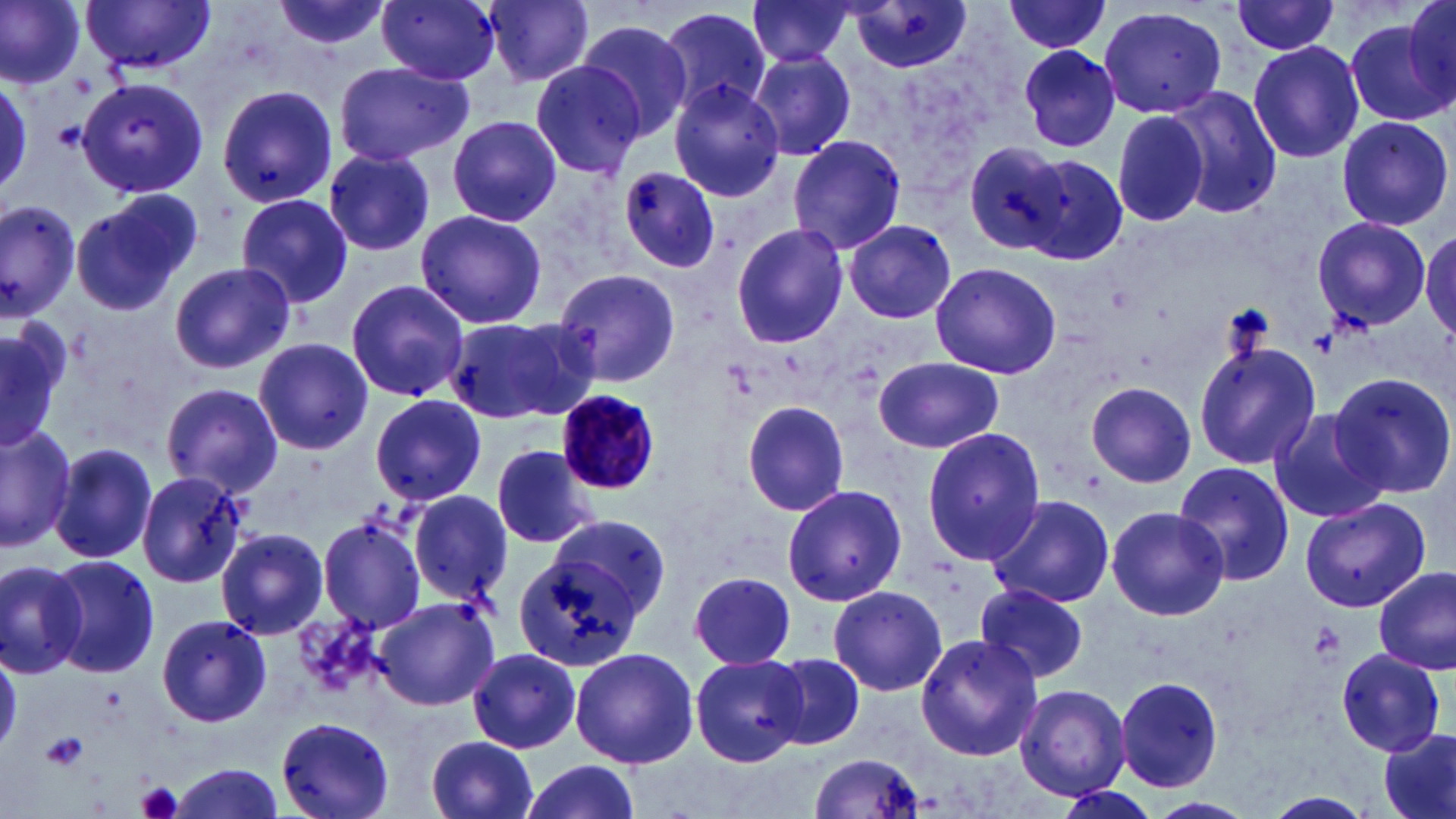
slide-level diagnosis = Plasmodium malariae
preparation = thin blood smear
modality = optical microscopy
field of view = single
platelet locations = approximate bounding boxes as named x1/y1/x2/y2 corners in pixels: (x1=54, y1=121, x2=86, y2=151), (x1=1309, y1=327, x2=1340, y2=356), (x1=1306, y1=623, x2=1344, y2=663), (x1=40, y1=732, x2=88, y2=770), (x1=134, y1=781, x2=185, y2=819)
magnification = 1000x
Plasmodium malariae-infected red blood cell locations = approximate bounding boxes as named x1/y1/x2/y2 corners in pixels: (x1=554, y1=388, x2=662, y2=496)
image size = 1456×819 pixels
uninfected red blood cell locations = approximate bounding boxes as named x1/y1/x2/y2 corners in pixels: (x1=0, y1=0, x2=87, y2=90), (x1=269, y1=0, x2=398, y2=55), (x1=378, y1=0, x2=502, y2=84), (x1=1403, y1=0, x2=1456, y2=104), (x1=83, y1=1, x2=218, y2=77), (x1=483, y1=1, x2=595, y2=86), (x1=1001, y1=1, x2=1114, y2=54), (x1=745, y1=2, x2=856, y2=66), (x1=1230, y1=2, x2=1342, y2=56), (x1=848, y1=4, x2=975, y2=74), (x1=1097, y1=5, x2=1229, y2=120), (x1=656, y1=6, x2=773, y2=121), (x1=1343, y1=14, x2=1452, y2=130), (x1=576, y1=22, x2=694, y2=142), (x1=1247, y1=41, x2=1364, y2=164), (x1=1017, y1=45, x2=1121, y2=153), (x1=748, y1=49, x2=857, y2=162), (x1=331, y1=60, x2=473, y2=166), (x1=528, y1=60, x2=648, y2=178), (x1=0, y1=75, x2=32, y2=196), (x1=77, y1=76, x2=210, y2=199), (x1=669, y1=81, x2=786, y2=202), (x1=216, y1=84, x2=339, y2=210), (x1=1164, y1=87, x2=1280, y2=218), (x1=1111, y1=110, x2=1208, y2=229), (x1=1335, y1=114, x2=1454, y2=232), (x1=447, y1=115, x2=562, y2=227), (x1=788, y1=134, x2=906, y2=254), (x1=960, y1=144, x2=1071, y2=254), (x1=322, y1=150, x2=441, y2=258), (x1=1015, y1=153, x2=1129, y2=267), (x1=617, y1=166, x2=723, y2=274), (x1=75, y1=189, x2=204, y2=314), (x1=235, y1=193, x2=354, y2=308), (x1=0, y1=201, x2=80, y2=320), (x1=414, y1=209, x2=549, y2=330), (x1=1311, y1=216, x2=1431, y2=328), (x1=843, y1=220, x2=957, y2=325), (x1=730, y1=223, x2=848, y2=349), (x1=1421, y1=226, x2=1456, y2=343), (x1=168, y1=261, x2=295, y2=374), (x1=927, y1=261, x2=1062, y2=380), (x1=551, y1=266, x2=684, y2=391), (x1=345, y1=279, x2=471, y2=403), (x1=444, y1=315, x2=594, y2=425), (x1=0, y1=320, x2=65, y2=456), (x1=253, y1=337, x2=372, y2=456), (x1=1194, y1=338, x2=1321, y2=468), (x1=874, y1=354, x2=1003, y2=453), (x1=1327, y1=373, x2=1456, y2=500), (x1=161, y1=381, x2=283, y2=497), (x1=1083, y1=381, x2=1197, y2=489), (x1=370, y1=393, x2=486, y2=505), (x1=741, y1=400, x2=848, y2=517), (x1=1267, y1=409, x2=1391, y2=524), (x1=0, y1=424, x2=78, y2=553), (x1=921, y1=426, x2=1046, y2=565), (x1=49, y1=441, x2=157, y2=565), (x1=492, y1=444, x2=600, y2=550), (x1=1172, y1=462, x2=1295, y2=587), (x1=136, y1=470, x2=249, y2=589), (x1=781, y1=483, x2=907, y2=607), (x1=409, y1=488, x2=513, y2=603), (x1=983, y1=493, x2=1116, y2=610), (x1=1300, y1=497, x2=1429, y2=611), (x1=1106, y1=506, x2=1230, y2=621), (x1=551, y1=513, x2=671, y2=618), (x1=317, y1=515, x2=429, y2=632), (x1=216, y1=527, x2=329, y2=639), (x1=510, y1=552, x2=634, y2=683), (x1=45, y1=554, x2=158, y2=678), (x1=0, y1=560, x2=88, y2=677), (x1=1374, y1=568, x2=1454, y2=674), (x1=688, y1=570, x2=797, y2=670), (x1=827, y1=584, x2=948, y2=697), (x1=975, y1=584, x2=1091, y2=684), (x1=374, y1=597, x2=500, y2=711), (x1=294, y1=611, x2=385, y2=697), (x1=156, y1=614, x2=272, y2=727), (x1=915, y1=633, x2=1043, y2=759), (x1=569, y1=646, x2=699, y2=768), (x1=1, y1=648, x2=22, y2=756), (x1=1334, y1=648, x2=1446, y2=756), (x1=469, y1=649, x2=582, y2=752), (x1=691, y1=653, x2=811, y2=767), (x1=767, y1=653, x2=864, y2=750), (x1=1113, y1=676, x2=1225, y2=792), (x1=1015, y1=684, x2=1132, y2=800), (x1=276, y1=716, x2=396, y2=819), (x1=1378, y1=727, x2=1455, y2=819), (x1=424, y1=735, x2=540, y2=819), (x1=808, y1=752, x2=926, y2=819), (x1=520, y1=758, x2=643, y2=819), (x1=165, y1=764, x2=287, y2=818), (x1=1053, y1=782, x2=1158, y2=819), (x1=1262, y1=791, x2=1378, y2=818), (x1=1147, y1=795, x2=1258, y2=819)
stain = May-Grünwald-Giemsa